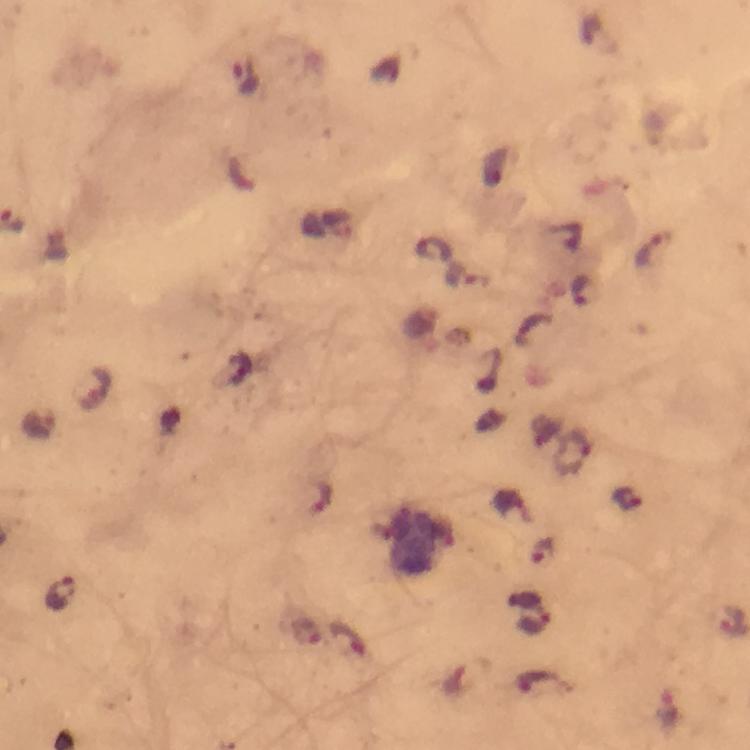 Approximate centers as [x, y] in pixels. Malaria parasite locations: [246, 75], [653, 249], [433, 250], [462, 276], [584, 289], [91, 390], [37, 423], [575, 454], [627, 497], [324, 498], [544, 551], [61, 593], [531, 610], [306, 634], [348, 638], [468, 678], [543, 683], [666, 711]. Thick blood smear. 100x magnification. Photographed through the microscope with a smartphone camera. From a diagnostic examination for malaria. Cropped region of a single field of view. Image is 750×750 pixels. Immersion oil was used. Giemsa-stained preparation.